Outline each Trypanosoma brucei.
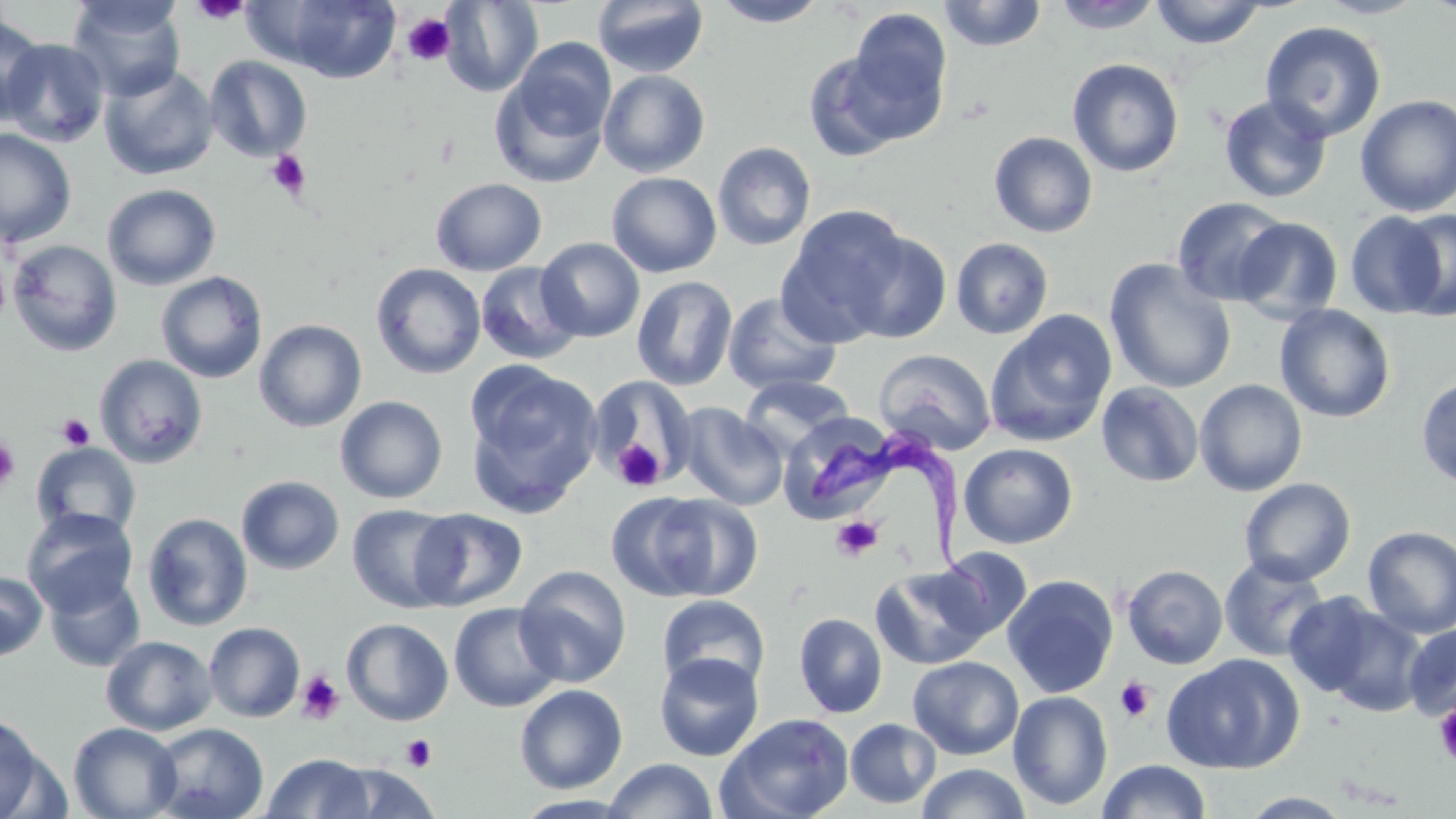
Approximate bounding boxes as named x1/y1/x2/y2 corners in pixels.
Trypanosoma brucei: (x1=811, y1=423, x2=1001, y2=608).

slide-level diagnosis = Trypanosoma brucei
preparation = thin blood smear
uninfected red blood cell locations = approximate bounding boxes as named x1/y1/x2/y2 corners in pixels: (x1=68, y1=0, x2=186, y2=101), (x1=257, y1=0, x2=404, y2=83), (x1=593, y1=0, x2=709, y2=78), (x1=711, y1=0, x2=828, y2=27), (x1=1313, y1=0, x2=1429, y2=19), (x1=439, y1=1, x2=543, y2=97), (x1=938, y1=1, x2=1048, y2=52), (x1=1048, y1=1, x2=1166, y2=33), (x1=1148, y1=1, x2=1268, y2=49), (x1=845, y1=9, x2=954, y2=137), (x1=0, y1=15, x2=47, y2=125), (x1=1260, y1=21, x2=1387, y2=141), (x1=1, y1=38, x2=110, y2=148), (x1=510, y1=38, x2=616, y2=141), (x1=803, y1=49, x2=916, y2=160), (x1=204, y1=56, x2=313, y2=162), (x1=1067, y1=58, x2=1184, y2=177), (x1=99, y1=64, x2=218, y2=180), (x1=489, y1=69, x2=612, y2=189), (x1=598, y1=70, x2=710, y2=177), (x1=1219, y1=94, x2=1333, y2=204), (x1=1354, y1=96, x2=1456, y2=216), (x1=0, y1=128, x2=77, y2=248), (x1=989, y1=131, x2=1098, y2=238), (x1=712, y1=142, x2=817, y2=251), (x1=607, y1=171, x2=722, y2=278), (x1=430, y1=177, x2=547, y2=276), (x1=102, y1=183, x2=221, y2=291), (x1=1172, y1=196, x2=1290, y2=306), (x1=777, y1=205, x2=912, y2=344), (x1=1345, y1=210, x2=1449, y2=318), (x1=1232, y1=217, x2=1344, y2=321), (x1=840, y1=227, x2=953, y2=344), (x1=536, y1=237, x2=645, y2=342), (x1=950, y1=237, x2=1054, y2=339), (x1=7, y1=239, x2=123, y2=357), (x1=1104, y1=259, x2=1237, y2=394), (x1=476, y1=262, x2=583, y2=364), (x1=371, y1=263, x2=486, y2=379), (x1=156, y1=271, x2=268, y2=383), (x1=632, y1=276, x2=738, y2=391), (x1=723, y1=292, x2=842, y2=396), (x1=1274, y1=304, x2=1396, y2=423), (x1=984, y1=310, x2=1118, y2=448), (x1=254, y1=319, x2=367, y2=433), (x1=874, y1=349, x2=997, y2=456), (x1=94, y1=354, x2=209, y2=468), (x1=465, y1=364, x2=603, y2=515), (x1=585, y1=373, x2=698, y2=485), (x1=741, y1=374, x2=854, y2=456), (x1=1416, y1=375, x2=1456, y2=489), (x1=1194, y1=379, x2=1308, y2=496), (x1=1096, y1=381, x2=1204, y2=487), (x1=335, y1=396, x2=448, y2=503), (x1=676, y1=403, x2=788, y2=510), (x1=781, y1=412, x2=903, y2=525), (x1=31, y1=441, x2=142, y2=539), (x1=958, y1=443, x2=1079, y2=549), (x1=236, y1=475, x2=344, y2=575), (x1=1239, y1=477, x2=1356, y2=586), (x1=638, y1=492, x2=764, y2=601), (x1=347, y1=504, x2=462, y2=614), (x1=21, y1=507, x2=139, y2=617), (x1=411, y1=507, x2=527, y2=611), (x1=142, y1=512, x2=253, y2=632), (x1=1361, y1=526, x2=1456, y2=638), (x1=928, y1=547, x2=1034, y2=645), (x1=1219, y1=554, x2=1330, y2=662), (x1=871, y1=564, x2=997, y2=670), (x1=1122, y1=564, x2=1229, y2=669), (x1=514, y1=565, x2=632, y2=687), (x1=0, y1=571, x2=47, y2=661), (x1=44, y1=572, x2=145, y2=672), (x1=1002, y1=575, x2=1119, y2=699), (x1=1283, y1=592, x2=1389, y2=699), (x1=657, y1=594, x2=770, y2=694), (x1=449, y1=602, x2=563, y2=713), (x1=1316, y1=605, x2=1426, y2=716), (x1=794, y1=613, x2=888, y2=719), (x1=341, y1=618, x2=454, y2=726), (x1=203, y1=622, x2=306, y2=723), (x1=1403, y1=622, x2=1456, y2=721), (x1=100, y1=635, x2=217, y2=736), (x1=654, y1=653, x2=764, y2=761), (x1=1162, y1=653, x2=1304, y2=774), (x1=907, y1=656, x2=1024, y2=760), (x1=514, y1=684, x2=628, y2=794), (x1=1008, y1=690, x2=1114, y2=811), (x1=716, y1=712, x2=855, y2=819), (x1=0, y1=715, x2=49, y2=819), (x1=845, y1=718, x2=941, y2=809), (x1=68, y1=722, x2=182, y2=819), (x1=148, y1=723, x2=268, y2=819), (x1=261, y1=752, x2=374, y2=818), (x1=602, y1=758, x2=719, y2=818), (x1=1098, y1=759, x2=1212, y2=818), (x1=330, y1=763, x2=440, y2=818), (x1=915, y1=763, x2=1032, y2=819), (x1=1238, y1=791, x2=1358, y2=818)
image size = 1456×819 pixels
modality = light microscopy
field of view = single
stain = May-Grünwald-Giemsa
platelet locations = approximate bounding boxes as named x1/y1/x2/y2 corners in pixels: (x1=190, y1=0, x2=251, y2=24), (x1=401, y1=13, x2=455, y2=66), (x1=266, y1=150, x2=311, y2=199), (x1=0, y1=253, x2=9, y2=326), (x1=56, y1=413, x2=95, y2=450), (x1=0, y1=437, x2=20, y2=490), (x1=612, y1=439, x2=666, y2=491), (x1=830, y1=516, x2=883, y2=561), (x1=296, y1=670, x2=345, y2=726), (x1=1114, y1=676, x2=1156, y2=723), (x1=1433, y1=702, x2=1456, y2=767), (x1=401, y1=734, x2=437, y2=771)
magnification = 1000x